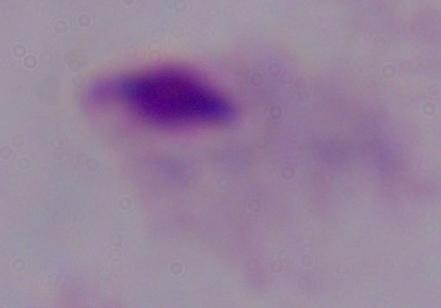
Micrograph. A trichomonad is seen. Captured at 1000x magnification.